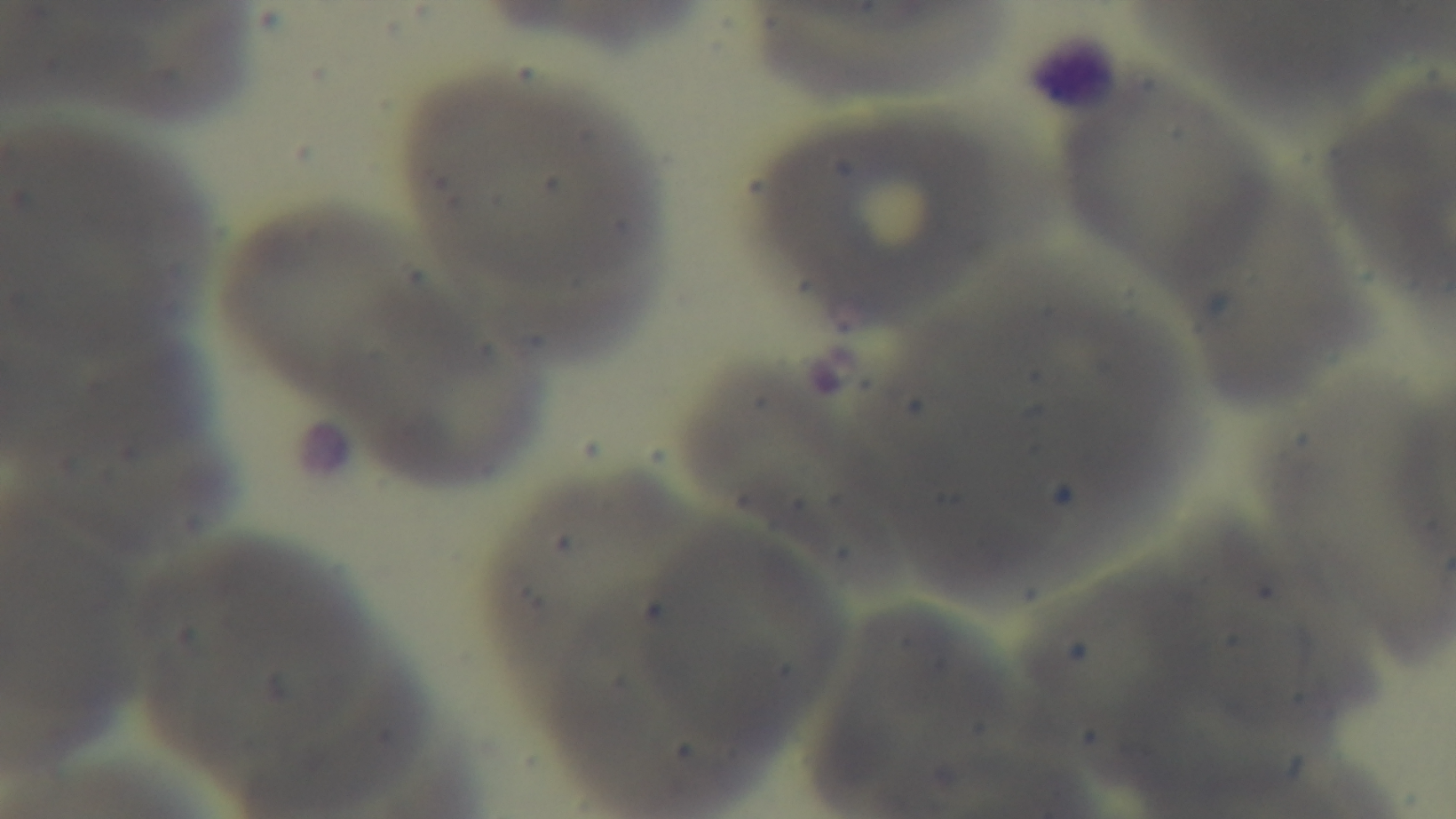

Summary:
  - Objective: 100x oil immersion
  - Malaria status: negative
  - Modality: light microscopy
  - Field of view: single
  - Preparation: thin
  - Capture: mounted 4K digital camera
  - Stain: Giemsa